Identify the preparation type.
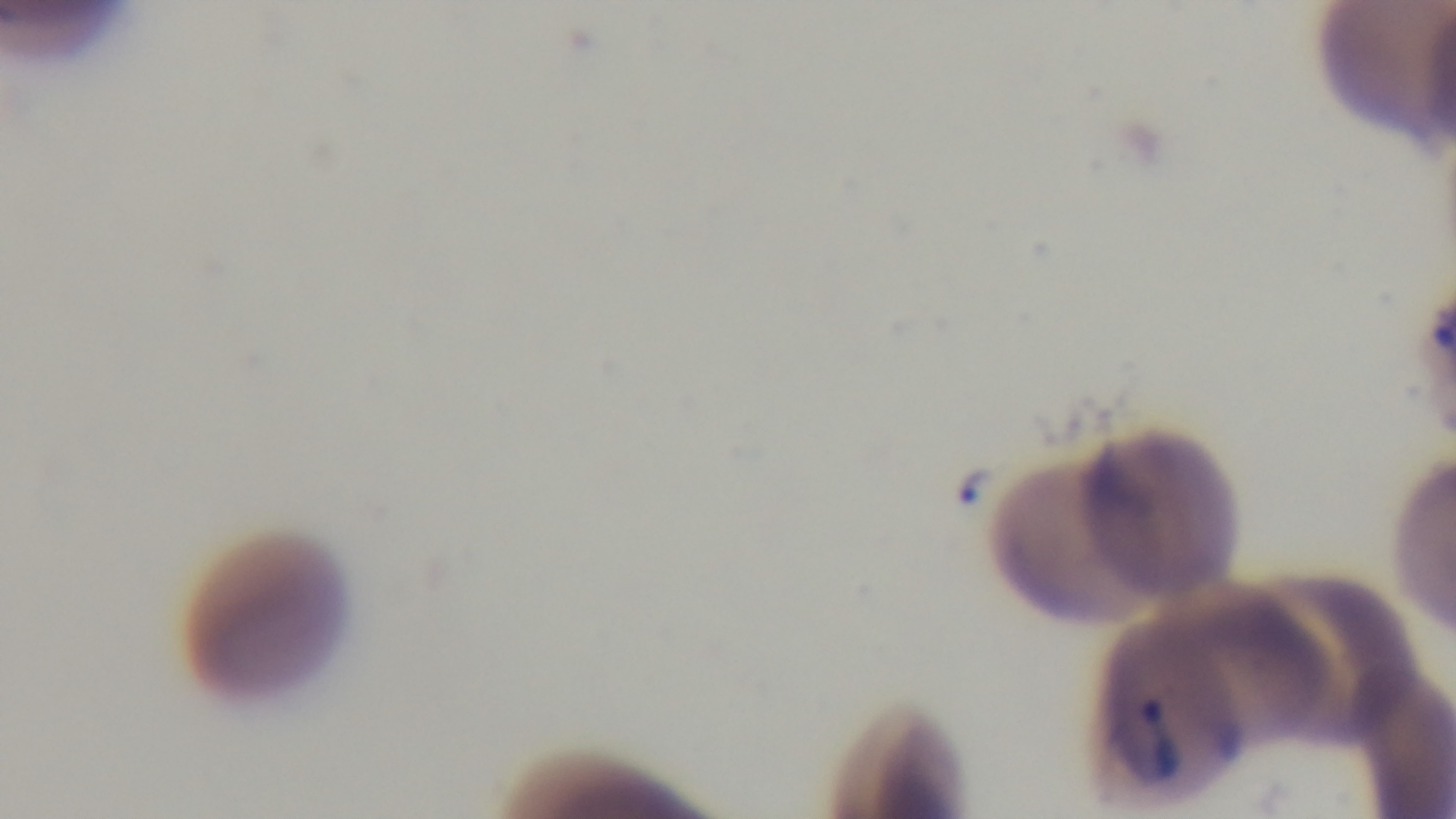
It is a thin blood film.

Malaria status: infected. Single field of view. Giemsa stain. 100x oil-immersion objective. Captured with a mounted 4K digital camera. Photomicrograph.